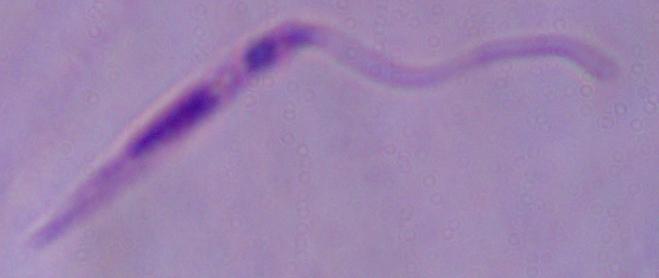
1000x magnification. Micrograph. A Leishmania parasite is seen.